Locate every leukocyte (white blood cell).
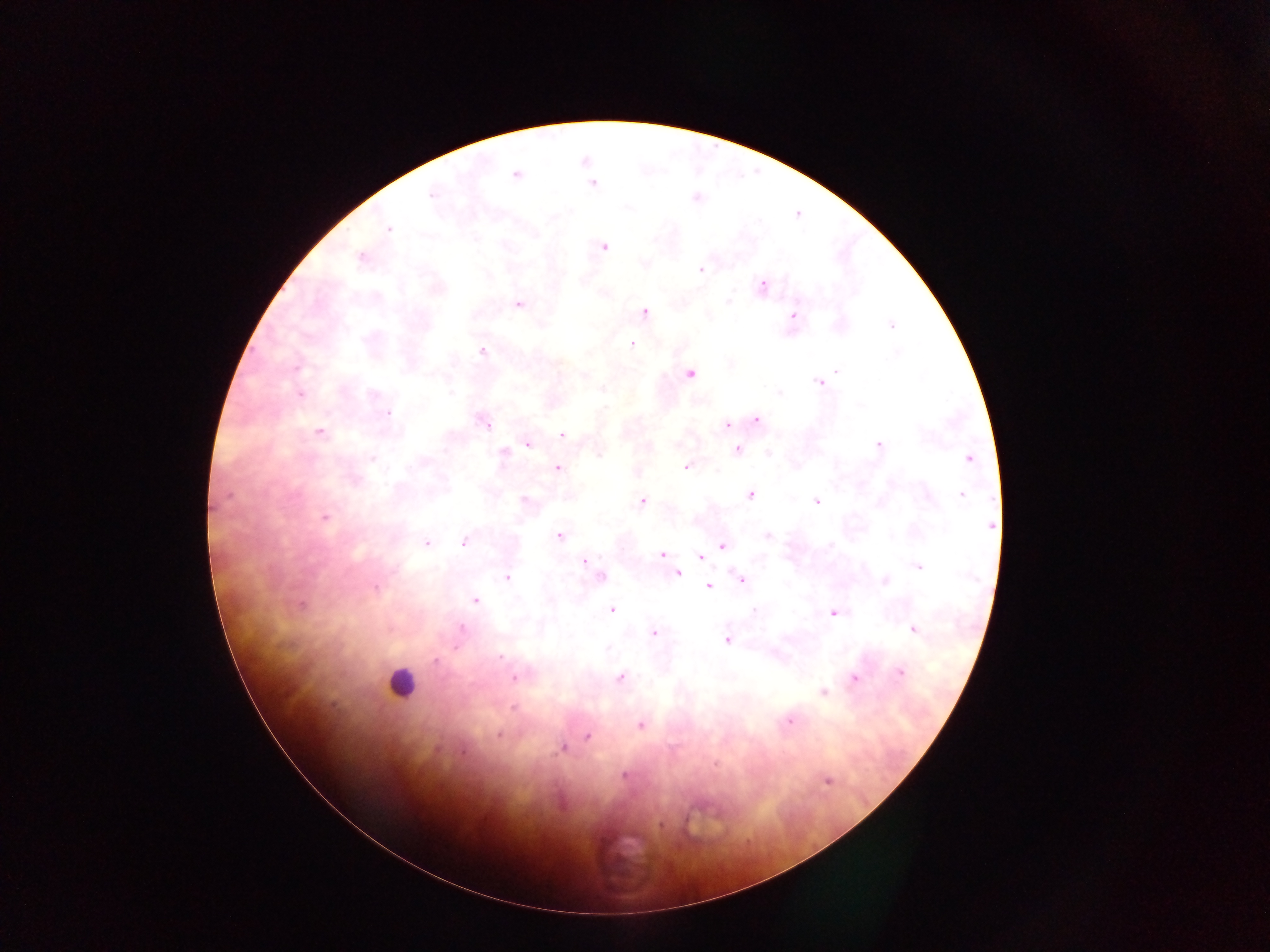

Approximate centers as (x, y) in pixels.
Leukocytes: (401, 683).

Summary:
  - Malaria parasite locations: (516, 175), (592, 184), (431, 195), (696, 197), (389, 228), (603, 247), (361, 257), (700, 270), (762, 286), (728, 301), (519, 305), (644, 312), (793, 316), (891, 325), (632, 343), (481, 350), (837, 371), (689, 374), (820, 382), (451, 393), (779, 393), (300, 395), (387, 414), (757, 420), (485, 422), (726, 425), (320, 432), (562, 434), (528, 445), (878, 445), (737, 450), (503, 453), (768, 453), (969, 458), (372, 459), (685, 467), (558, 468), (750, 494), (961, 494), (227, 495), (525, 500), (642, 501), (816, 501), (325, 516), (990, 525), (768, 536), (558, 537), (464, 541), (426, 543), (722, 546), (661, 555), (701, 557), (584, 562), (919, 567), (677, 573), (601, 577), (507, 578), (742, 580), (884, 581), (709, 586), (375, 588), (475, 600), (302, 604), (612, 609), (753, 610), (834, 613), (461, 629), (914, 630), (654, 633), (726, 640), (501, 657), (436, 660), (900, 673), (514, 678), (621, 678), (854, 678), (824, 692), (514, 708), (790, 721), (640, 725), (498, 735), (588, 736), (562, 749), (625, 776), (827, 781), (662, 825)
  - Image size: 1270×952 pixels
  - Capture: mobile-phone photograph through a microscope
  - Field of view: single
  - Country: Ghana
  - Preparation: thick blood smear